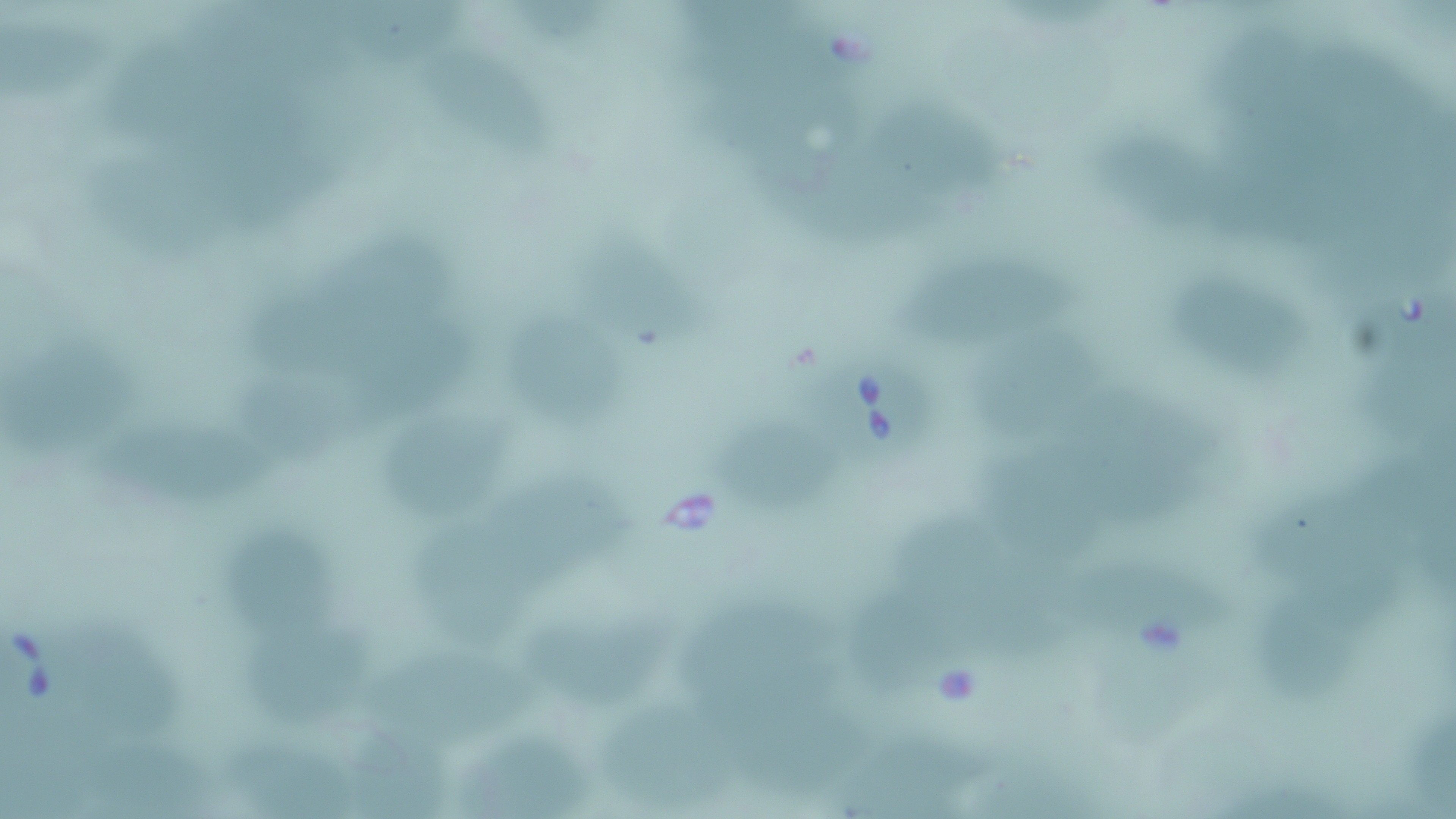
Summary:
  - Coordinate format: approximate bounding boxes as (x1,y1)-(x2,y2) corner pairs in pixels
  - Babesia divergens-infected red blood cell locations: (808,344)-(934,473), (1,617)-(86,719)
  - Uninfected red blood cell locations: (344,0)-(473,74), (3,13)-(109,108), (109,37)-(217,153), (448,51)-(556,170), (715,76)-(881,192), (881,97)-(1015,204), (1109,143)-(1240,239), (1232,144)-(1354,247), (91,148)-(237,270), (811,152)-(959,253), (336,234)-(462,330), (575,235)-(716,379), (896,263)-(1071,352), (1185,277)-(1317,396), (245,289)-(383,381), (509,314)-(633,436), (373,322)-(487,420), (985,330)-(1110,443), (1370,334)-(1451,473), (3,341)-(134,459), (247,380)-(374,471), (1091,395)-(1231,493), (393,413)-(531,514), (716,422)-(842,506), (117,430)-(279,511), (1004,466)-(1131,566), (488,472)-(643,581), (1271,502)-(1390,586), (906,515)-(1034,619), (432,530)-(538,637), (239,531)-(338,650), (1090,573)-(1245,655), (985,582)-(1098,683), (1251,586)-(1377,704), (682,589)-(849,721), (865,600)-(969,703), (521,607)-(678,719), (82,623)-(181,741), (261,640)-(378,731), (382,652)-(551,741), (1404,692)-(1456,809), (739,695)-(869,786), (606,703)-(719,812), (457,725)-(593,818), (355,727)-(438,813), (855,730)-(999,814), (235,737)-(363,819), (98,745)-(204,819)
  - Slide-level diagnosis: Babesia divergens
  - Magnification: 1000x
  - Preparation: thin blood smear
  - Field of view: single
  - Image size: 1456×819 pixels
  - Modality: optical microscopy
  - Stain: May-Grünwald-Giemsa